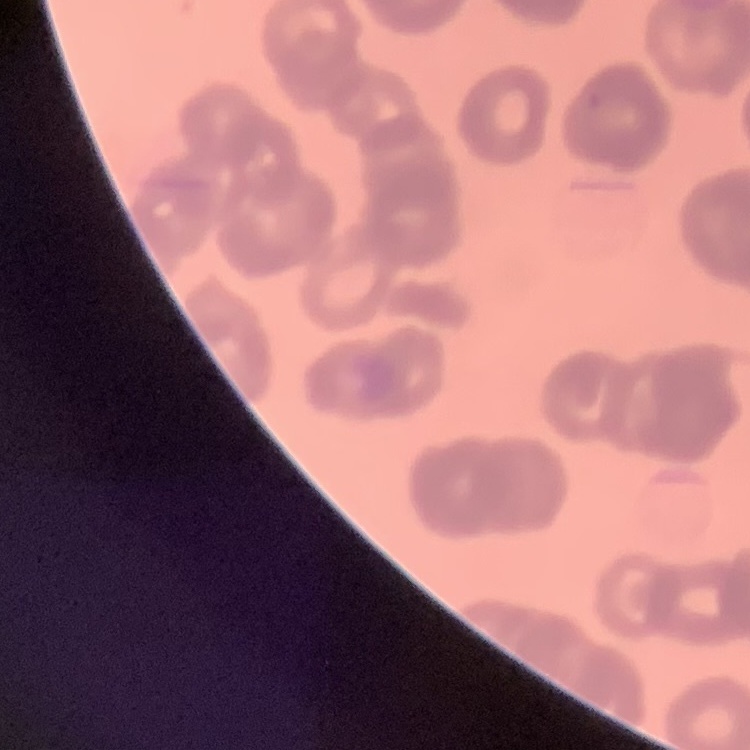

red blood cell morphology = rouleaux formation
image type = square crop of a larger photomicrograph
preparation = thin blood film
stain = Field's or Giemsa